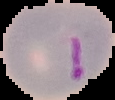
{
  "image_size": "115×100 pixels",
  "preparation": "thin blood film",
  "image_type": "segmented cell region on a black background",
  "malaria_status": "parasitized"
}